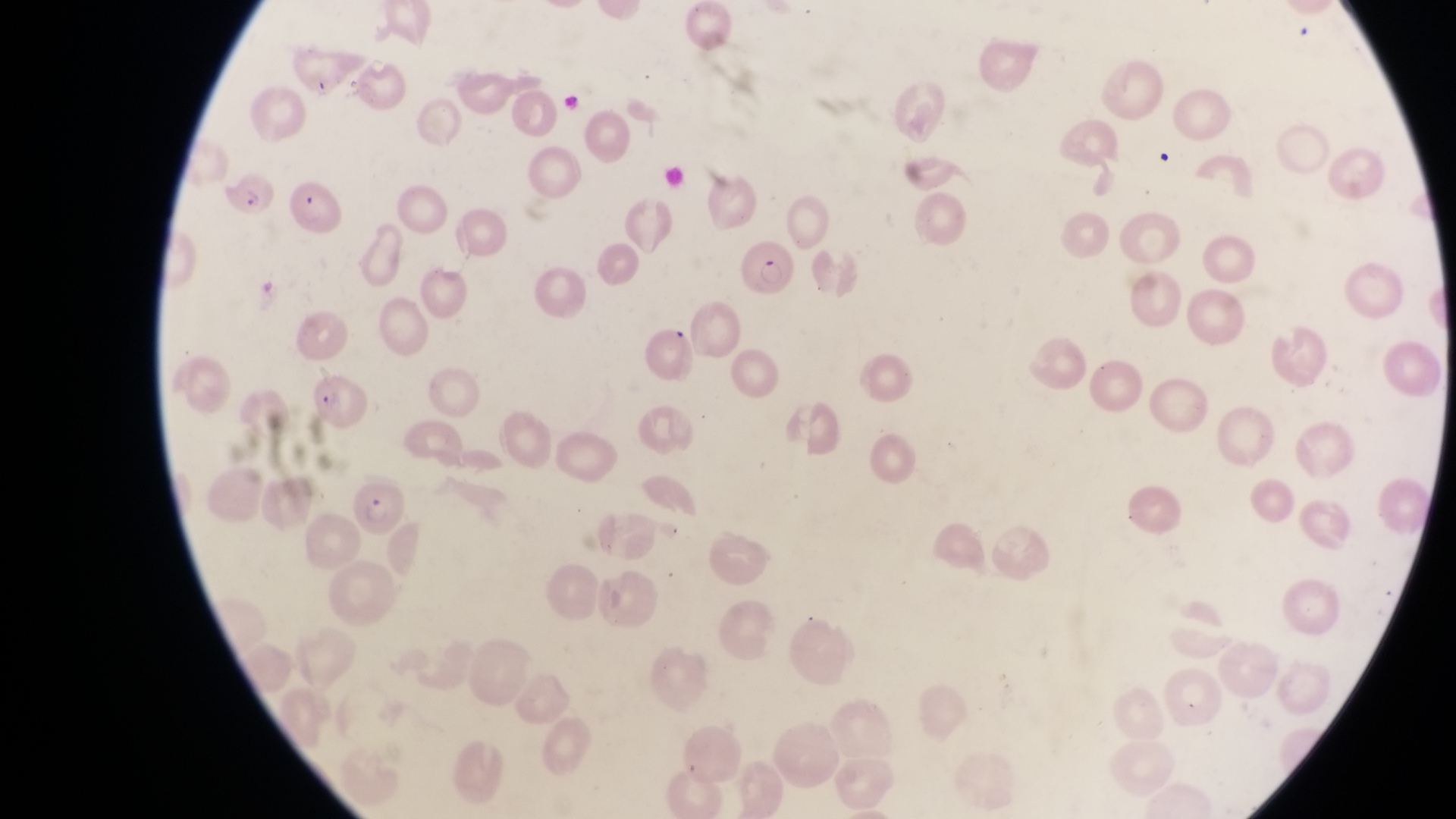
Approximate bounding boxes as left top right bottom in pixels.
Summary:
  - Parasitised red blood cell locations: 224 164 276 223; 735 240 795 304; 304 364 371 433; 347 485 405 538
  - Capture: smartphone photograph through the eyepiece of an Olympus CX-23 microscope
  - Image size: 1456×819 pixels
  - Country: Uganda
  - Magnification: 1000x
  - Field of view: single
  - Preparation: thin blood film